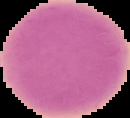

Summary:
  - Result: negative for malaria parasites
  - Image size: 130×118 pixels
  - Preparation: thin blood film
  - Image type: segmented cell region on a black background